Give the preparation type.
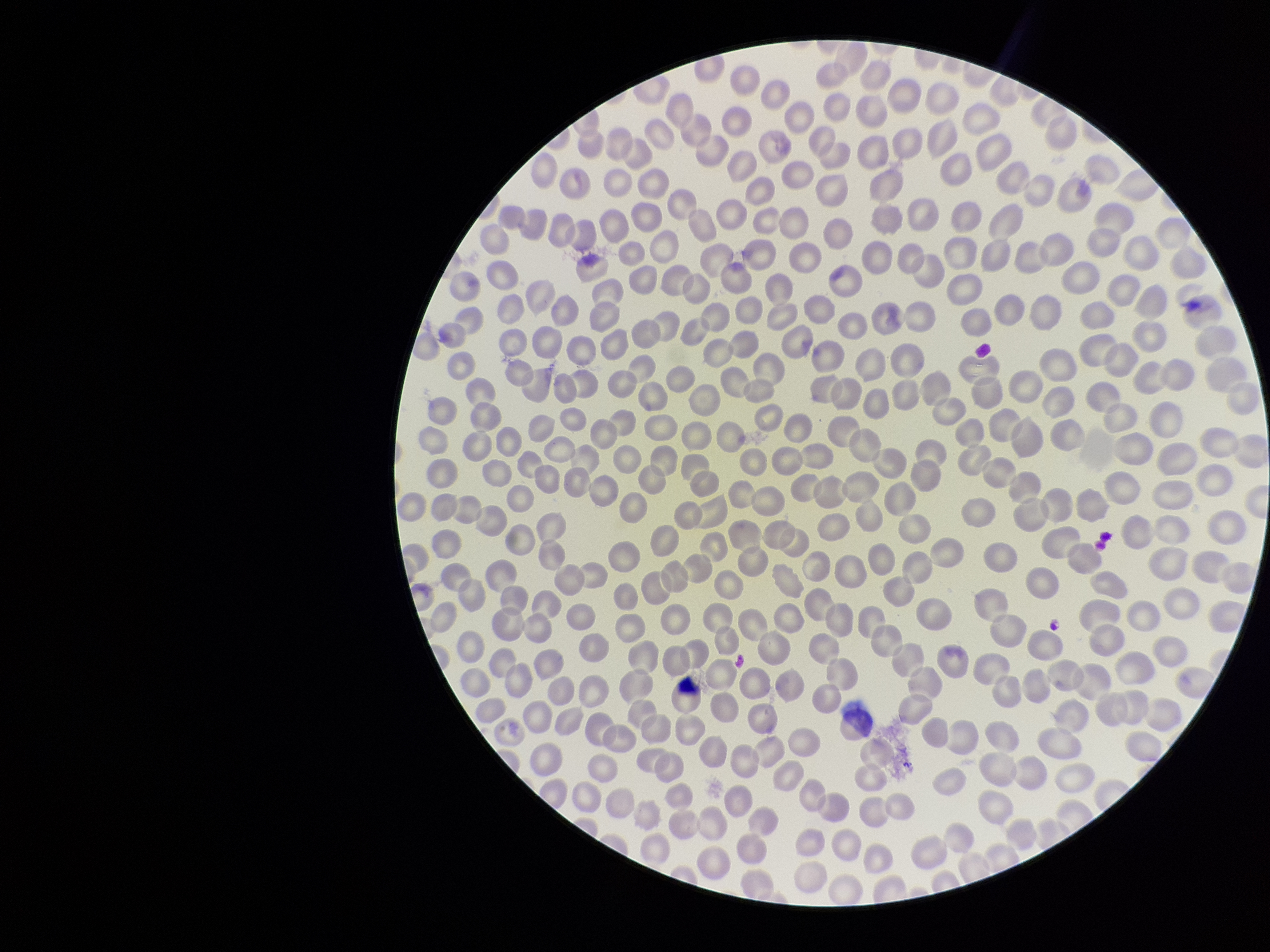

Thin.

field of view = single
image size = 1270×952 pixels
parasitized red blood cell count = 0
stain = Giemsa
patient malaria status = negative
red blood cell count = 352
capture = smartphone photograph through the microscope eyepiece
parasitized red blood cells = none seen